Report the malaria status of this cell.
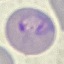

It is parasitized.

preparation = thin blood smear
image type = cell patch, automatically extracted from a larger field of view and resized to 64 × 64 pixels
capture = smartphone through the microscope eyepiece
stain = Giemsa